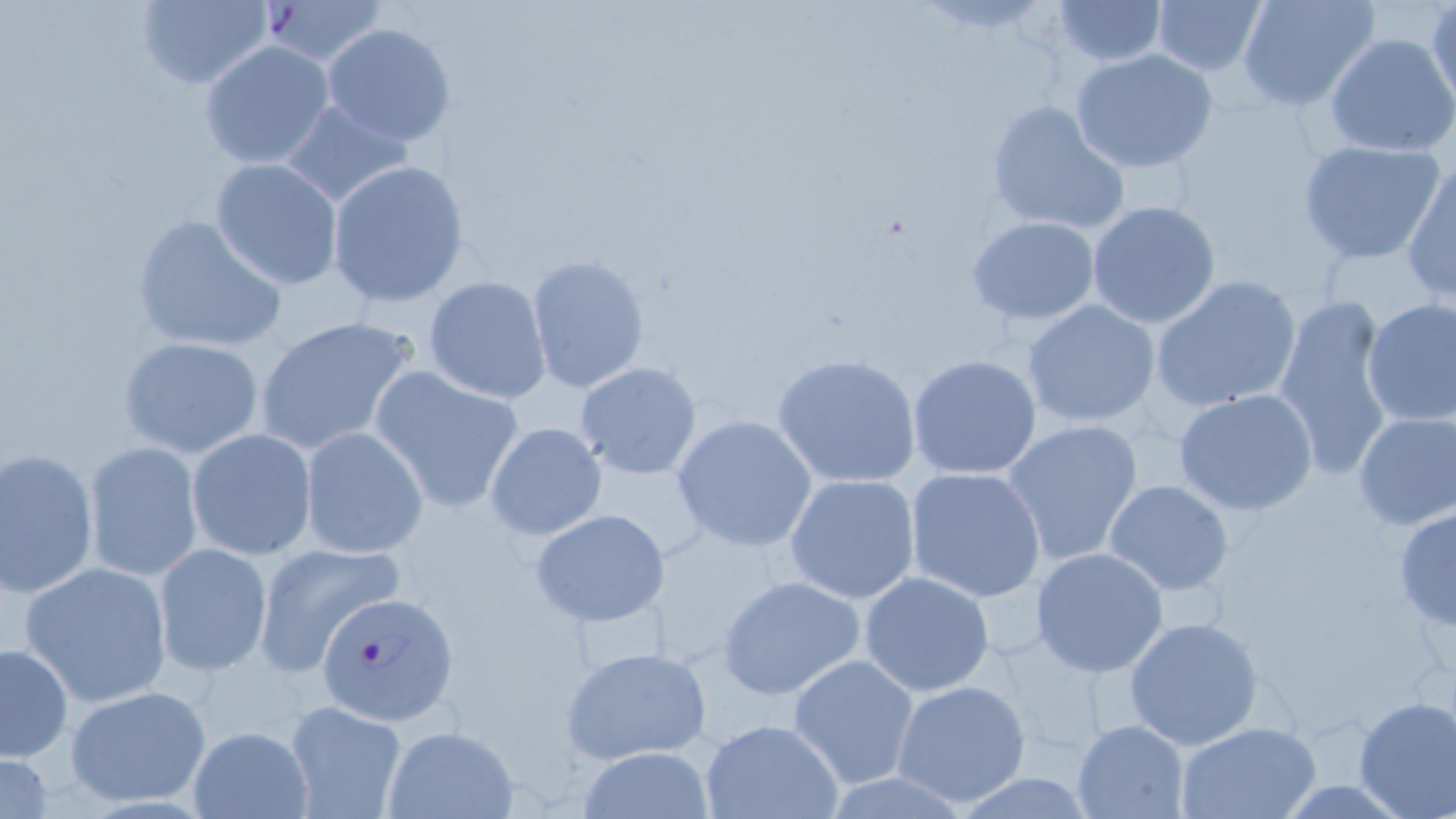

Summary:
  - Coordinate format: approximate bounding boxes as (x1,y1)-(x2,y2) corner pairs in pixels
  - Plasmodium falciparum-infected red blood cell locations: (317,591)-(460,725)
  - Uninfected red blood cell locations: (1047,0)-(1168,66), (1236,0)-(1380,112), (135,1)-(273,89), (253,1)-(389,65), (1151,1)-(1266,77), (1427,1)-(1456,112), (322,22)-(457,145), (1325,34)-(1456,156), (199,41)-(335,170), (1069,48)-(1219,173), (279,98)-(413,208), (985,99)-(1130,238), (1296,139)-(1446,265), (209,159)-(344,290), (326,160)-(470,307), (1402,160)-(1455,306), (1086,200)-(1222,330), (130,214)-(286,355), (967,216)-(1101,327), (526,254)-(651,395), (425,275)-(551,403), (1150,275)-(1303,415), (1272,296)-(1394,476), (1360,298)-(1456,427), (1021,299)-(1164,428), (253,314)-(420,455), (117,336)-(264,459), (772,352)-(923,489), (907,354)-(1041,480), (574,362)-(703,481), (368,366)-(525,514), (1173,387)-(1319,517), (1351,410)-(1456,531), (671,414)-(818,553), (1002,418)-(1145,566), (483,420)-(608,542), (300,428)-(428,559), (187,429)-(317,560), (83,441)-(203,583), (1,447)-(99,597), (903,466)-(1046,602), (784,473)-(921,603), (1102,479)-(1235,597), (1393,506)-(1456,633), (530,509)-(673,628), (253,540)-(405,676), (154,543)-(273,677), (1029,548)-(1170,679), (18,560)-(174,709), (859,570)-(995,696), (716,574)-(869,701), (1123,617)-(1264,752), (0,643)-(72,767), (559,645)-(713,765), (788,653)-(920,789), (892,679)-(1034,808), (64,684)-(212,807), (1352,696)-(1456,819), (283,700)-(408,819), (698,718)-(845,819), (1070,719)-(1189,818), (1175,721)-(1323,818), (381,726)-(518,818), (185,727)-(315,818), (577,746)-(713,818), (0,748)-(53,819)
  - Slide-level diagnosis: Plasmodium falciparum
  - Preparation: thin blood smear
  - Image size: 1456×819 pixels
  - Magnification: 1000x
  - Stain: May-Grünwald-Giemsa
  - Field of view: single
  - Modality: light microscopy